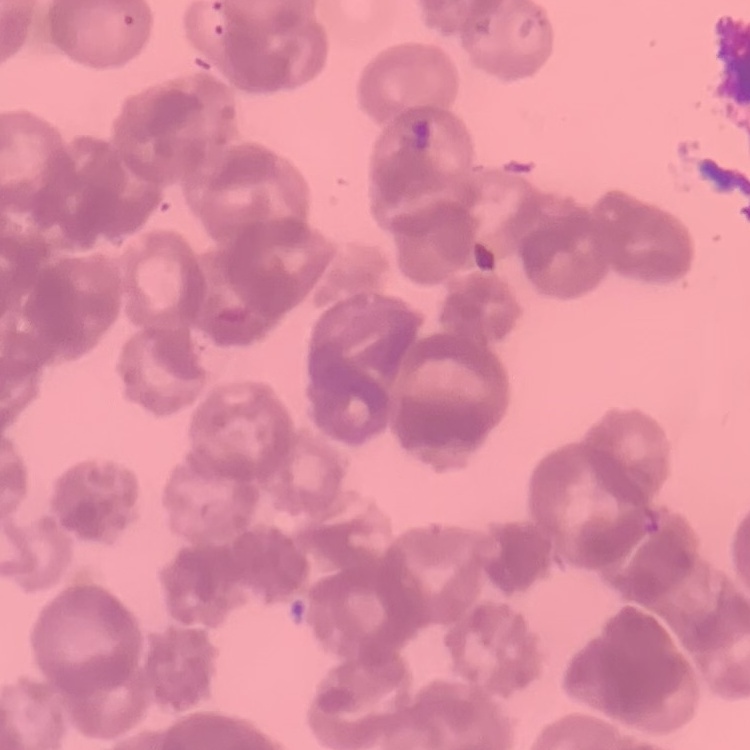
{
  "red_blood_cell_morphology": "rouleaux formation",
  "stain": "Field's or Giemsa",
  "image_type": "square crop of a larger photomicrograph",
  "preparation": "thin blood film"
}